State which cell type is depicted.
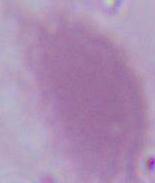
An erythrocyte.

Summary:
  - Modality: photomicrograph
  - Magnification: 1000x